Name the parasite shown.
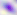
This is Toxoplasma gondii.

{
  "magnification": "400x",
  "modality": "photomicrograph"
}